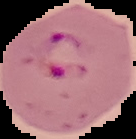
Result: malaria parasites detected. Segmented cell region on a black background. From a thin blood film. Image is 136×139 pixels.